Comment on the morphology of the erythrocytes.
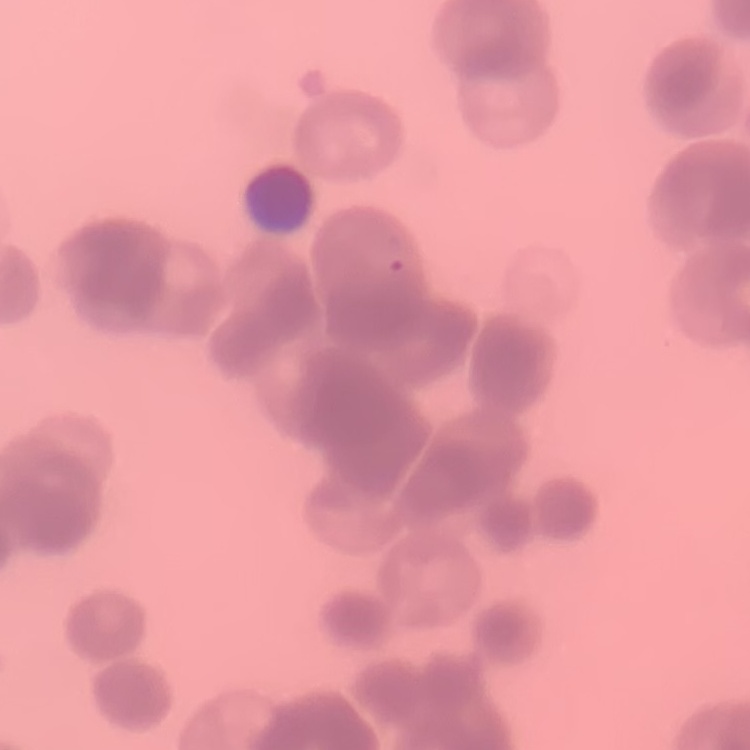
Rouleaux formation.

{
  "preparation": "thin blood smear",
  "image_type": "one tile cut from a larger photomicrograph",
  "stain": "Field's or Giemsa"
}